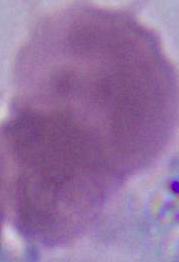
1000x magnification. Photomicrograph. An erythrocyte is shown.